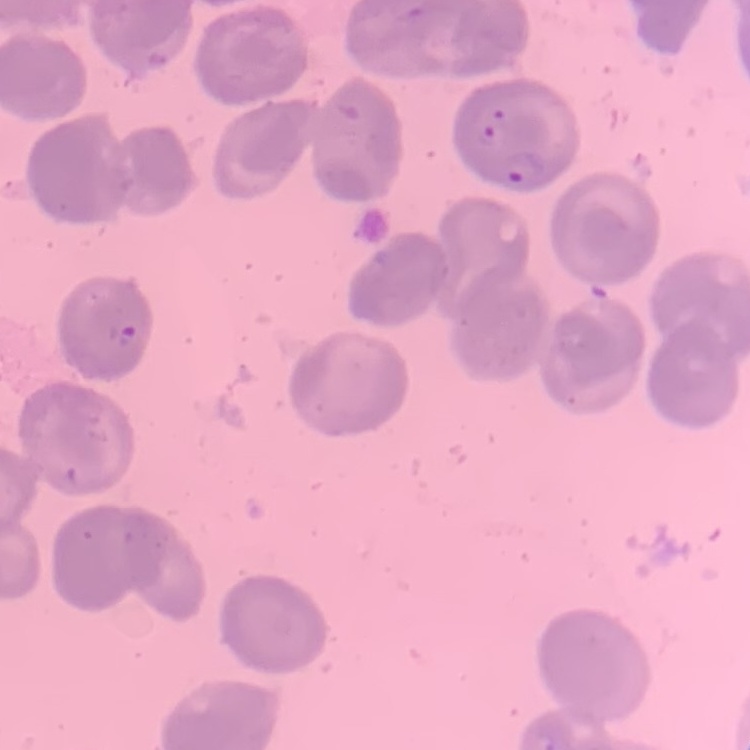
erythrocyte_morphology: no rouleaux formation
image_type: square crop of a larger photomicrograph
stain: Field's or Giemsa
preparation: thin blood film